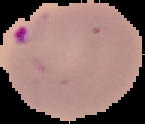

result = Plasmodium parasites identified
image size = 145×124 pixels
image type = cell region segmented out of the field of view; surrounding area masked to black
preparation = thin blood smear